Identify the parasite.
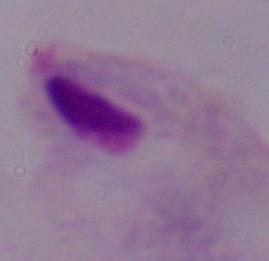
A trichomonad.

Micrograph. Captured at 1000x magnification.